Assess this cell for malaria.
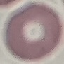
Uninfected.

Summary:
  - Image type: cell patch, automatically extracted from a larger field of view and resized to 64 × 64 pixels
  - Stain: Giemsa
  - Preparation: thin blood film
  - Capture: smartphone through the microscope eyepiece